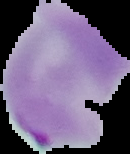

Image is 130×154 pixels. The area outside the segmented cell region is set to black. From a thin blood smear. Malaria status: parasitized.